Report the malaria status of this cell.
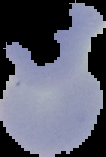
It is uninfected.

Image is 106×157 pixels. Cell region segmented out of the field of view; the surrounding area is masked to black. From a thin blood film.